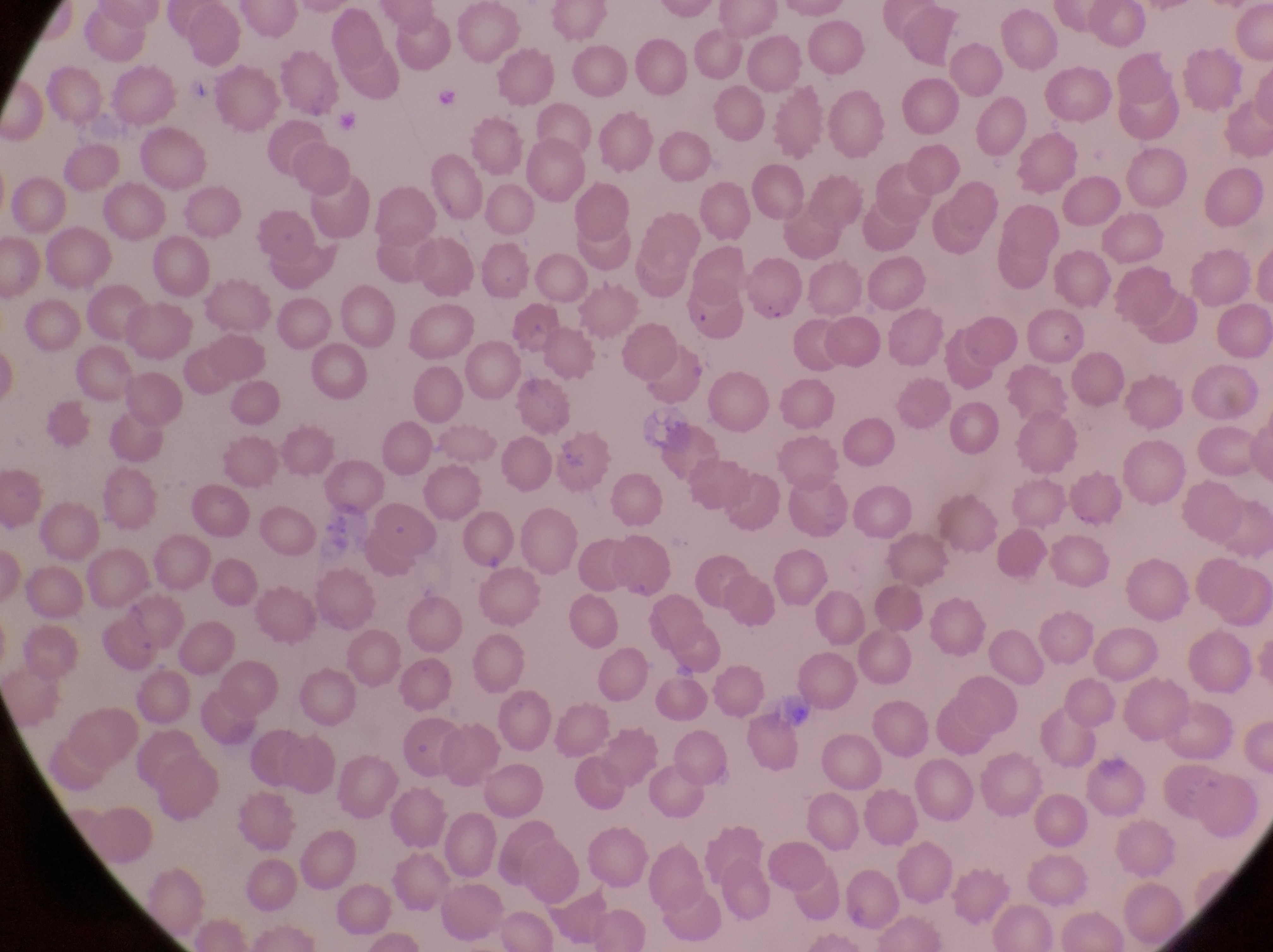
image_size: 1273×952 pixels
capture: smartphone photograph through the eyepiece of an Olympus CX-23 microscope
magnification: 1000x
parasitised_red_blood_cell_locations: 'approximate bounding boxes as [left, top, right, bottom] in pixels: [746, 255, 809, 322]'
field_of_view: single
country: Uganda
preparation: thin blood film